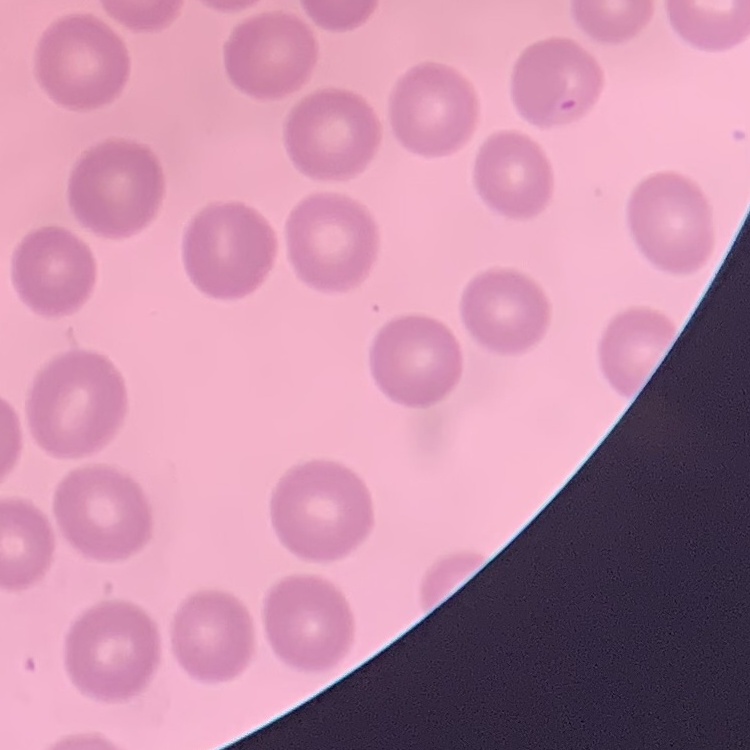
Summary:
  - Red blood cell morphology: no rouleaux formation
  - Preparation: thin blood film
  - Stain: Field's or Giemsa
  - Image type: one tile cut from a larger photomicrograph